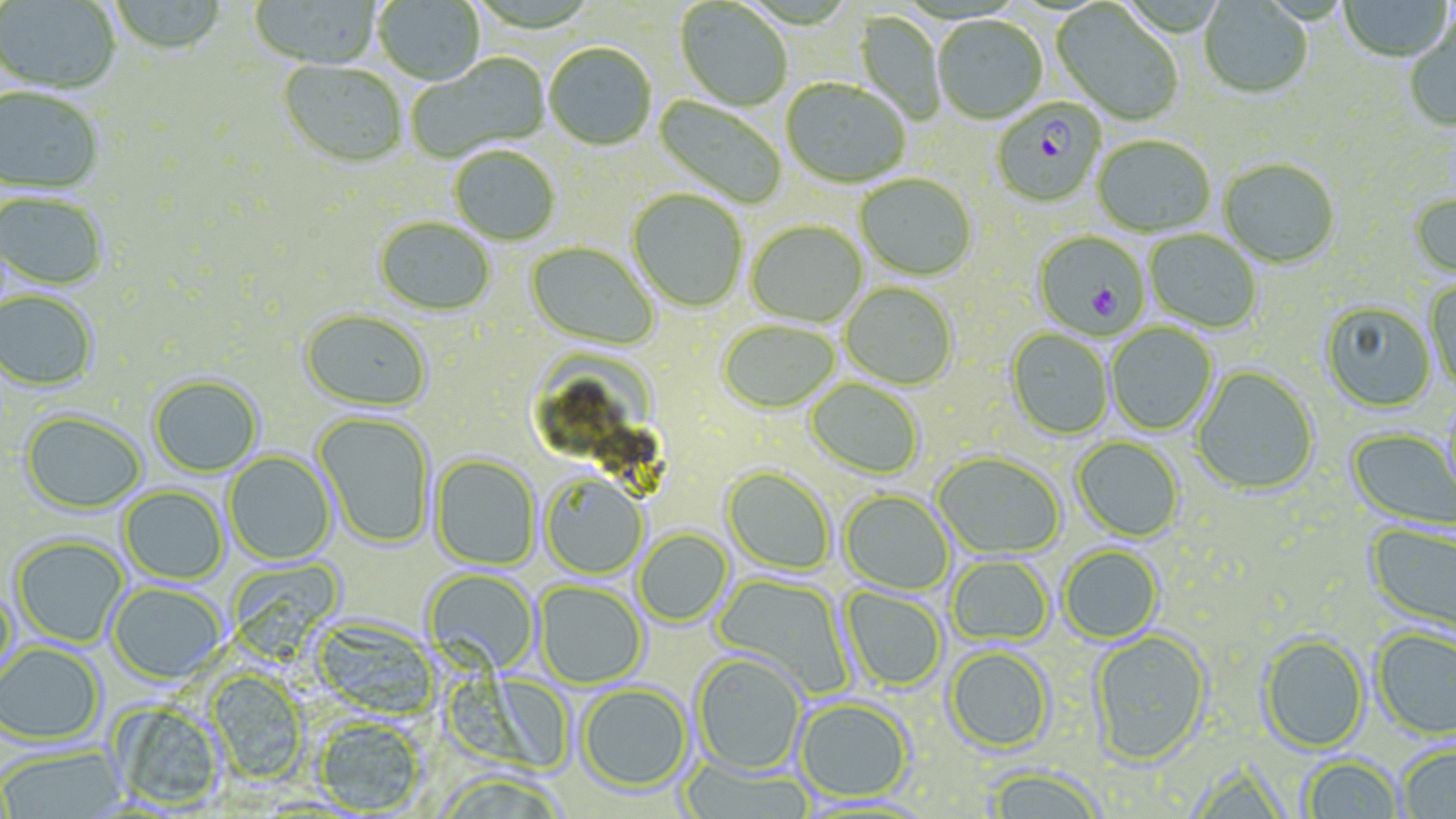
Summary:
  - Coordinate format: approximate bounding boxes as (x1, y1, x2, y2) in pixels
  - Plasmodium falciparum-infected red blood cell locations: (991, 100, 1106, 209), (1034, 230, 1151, 339)
  - Uninfected red blood cell locations: (110, 0, 228, 57), (248, 0, 383, 71), (373, 0, 486, 87), (1339, 0, 1453, 63), (1, 1, 121, 97), (674, 1, 792, 112), (1199, 1, 1312, 100), (1051, 3, 1184, 125), (853, 11, 946, 125), (1405, 14, 1456, 131), (932, 17, 1048, 127), (544, 44, 657, 152), (406, 53, 551, 164), (278, 61, 407, 170), (781, 80, 910, 189), (0, 88, 103, 197), (651, 94, 788, 208), (1092, 137, 1215, 238), (450, 147, 561, 247), (1219, 160, 1340, 270), (854, 174, 976, 281), (627, 190, 748, 313), (0, 193, 109, 293), (1409, 194, 1456, 281), (374, 218, 495, 318), (746, 221, 867, 328), (1144, 230, 1261, 334), (524, 242, 659, 352), (1425, 280, 1456, 393), (841, 283, 957, 390), (0, 292, 98, 393), (1320, 302, 1436, 413), (298, 311, 432, 414), (718, 321, 840, 415), (1106, 324, 1217, 436), (1006, 330, 1113, 440), (1191, 366, 1319, 496), (149, 376, 263, 478), (805, 378, 924, 480), (20, 413, 147, 516), (314, 413, 435, 550), (1346, 428, 1456, 532), (1072, 437, 1184, 542), (224, 451, 336, 566), (932, 453, 1065, 560), (430, 455, 540, 571), (722, 467, 835, 576), (540, 474, 647, 581), (118, 487, 228, 586), (839, 491, 953, 596), (1365, 522, 1456, 639), (634, 529, 733, 627), (11, 536, 129, 649), (1059, 546, 1163, 644), (947, 556, 1054, 646), (225, 557, 345, 662), (422, 569, 540, 677), (711, 573, 854, 698), (1, 581, 19, 687), (534, 581, 648, 689), (108, 583, 227, 686), (839, 586, 947, 692), (312, 618, 440, 720), (1372, 628, 1456, 740), (1089, 630, 1212, 766), (1258, 635, 1369, 753), (0, 643, 104, 746), (944, 646, 1055, 754), (692, 653, 807, 776), (206, 671, 308, 785), (578, 684, 692, 794), (795, 698, 914, 802), (107, 701, 225, 811), (313, 718, 426, 815), (1398, 745, 1456, 818), (0, 746, 127, 818), (1300, 755, 1403, 818), (679, 758, 814, 819), (984, 767, 1105, 819)
  - Slide-level diagnosis: Plasmodium falciparum
  - Modality: light microscopy
  - Image size: 1456×819 pixels
  - Magnification: 1000x
  - Field of view: single
  - Stain: May-Grünwald-Giemsa
  - Preparation: thin blood smear